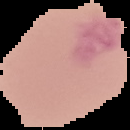

Summary:
  - Preparation: thin blood film
  - Image type: segmented cell region with the area outside set to black
  - Malaria status: uninfected
  - Image size: 130×130 pixels